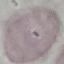

Summary:
  - Malaria status: uninfected
  - Capture: smartphone through the microscope eyepiece
  - Preparation: thin blood film
  - Stain: Giemsa
  - Image type: cell patch, automatically extracted from a larger field of view and resized to 64 × 64 pixels